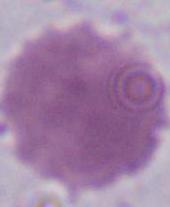
An erythrocyte is shown. Photomicrograph. Captured at 1000x magnification.